Locate every Plasmodium falciparum-infected red blood cell.
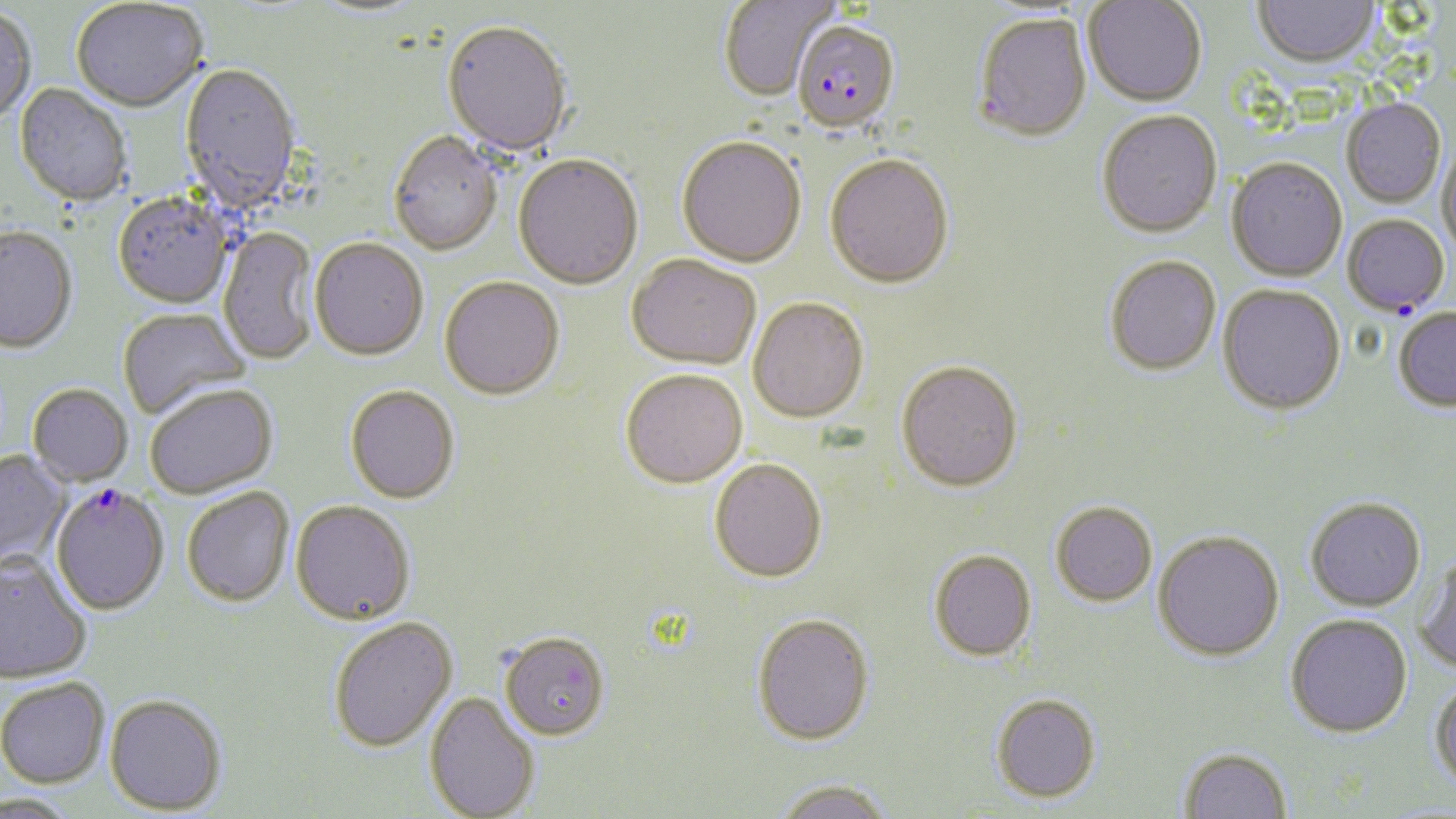

Approximate bounding boxes as (x1, y1, x2, y2) in pixels.
Plasmodium falciparum-infected red blood cells: (792, 22, 900, 137), (1342, 215, 1449, 316), (50, 487, 169, 616).

slide-level diagnosis = Plasmodium falciparum
stain = May-Grünwald-Giemsa
preparation = thin blood film
modality = light microscopy
magnification = 1000x
image size = 1456×819 pixels
field of view = single
uninfected red blood cell locations = approximate bounding boxes as (x1, y1, x2, y2) in pixels: (718, 0, 839, 103), (1253, 0, 1379, 71), (1083, 1, 1207, 109), (71, 2, 208, 115), (308, 2, 429, 22), (0, 9, 37, 126), (973, 15, 1093, 145), (442, 24, 572, 159), (180, 64, 303, 213), (14, 84, 132, 209), (1341, 99, 1445, 208), (1097, 112, 1222, 241), (388, 134, 502, 258), (676, 139, 807, 270), (1437, 140, 1456, 257), (513, 157, 643, 292), (824, 157, 954, 293), (1226, 160, 1347, 284), (113, 195, 235, 311), (0, 228, 78, 356), (218, 229, 318, 365), (310, 241, 428, 363), (626, 257, 761, 372), (1105, 258, 1221, 378), (439, 279, 564, 402), (1217, 285, 1346, 417), (748, 299, 869, 426), (1392, 308, 1456, 412), (117, 309, 252, 420), (896, 364, 1023, 496), (621, 372, 747, 491), (27, 385, 132, 488), (145, 386, 279, 500), (345, 387, 460, 506), (0, 450, 71, 568), (710, 461, 827, 585), (182, 488, 295, 609), (1305, 497, 1426, 612), (291, 502, 416, 626), (1051, 503, 1157, 607), (1153, 531, 1284, 661), (929, 550, 1037, 663), (0, 553, 92, 685), (1414, 555, 1456, 675), (1285, 614, 1412, 737), (751, 615, 875, 745), (329, 617, 458, 753), (500, 632, 610, 741), (1429, 675, 1456, 792), (0, 677, 110, 788), (424, 691, 540, 819), (105, 693, 227, 815), (991, 693, 1101, 803), (1179, 746, 1293, 819), (773, 778, 897, 819), (0, 793, 78, 819)